State the preparation type.
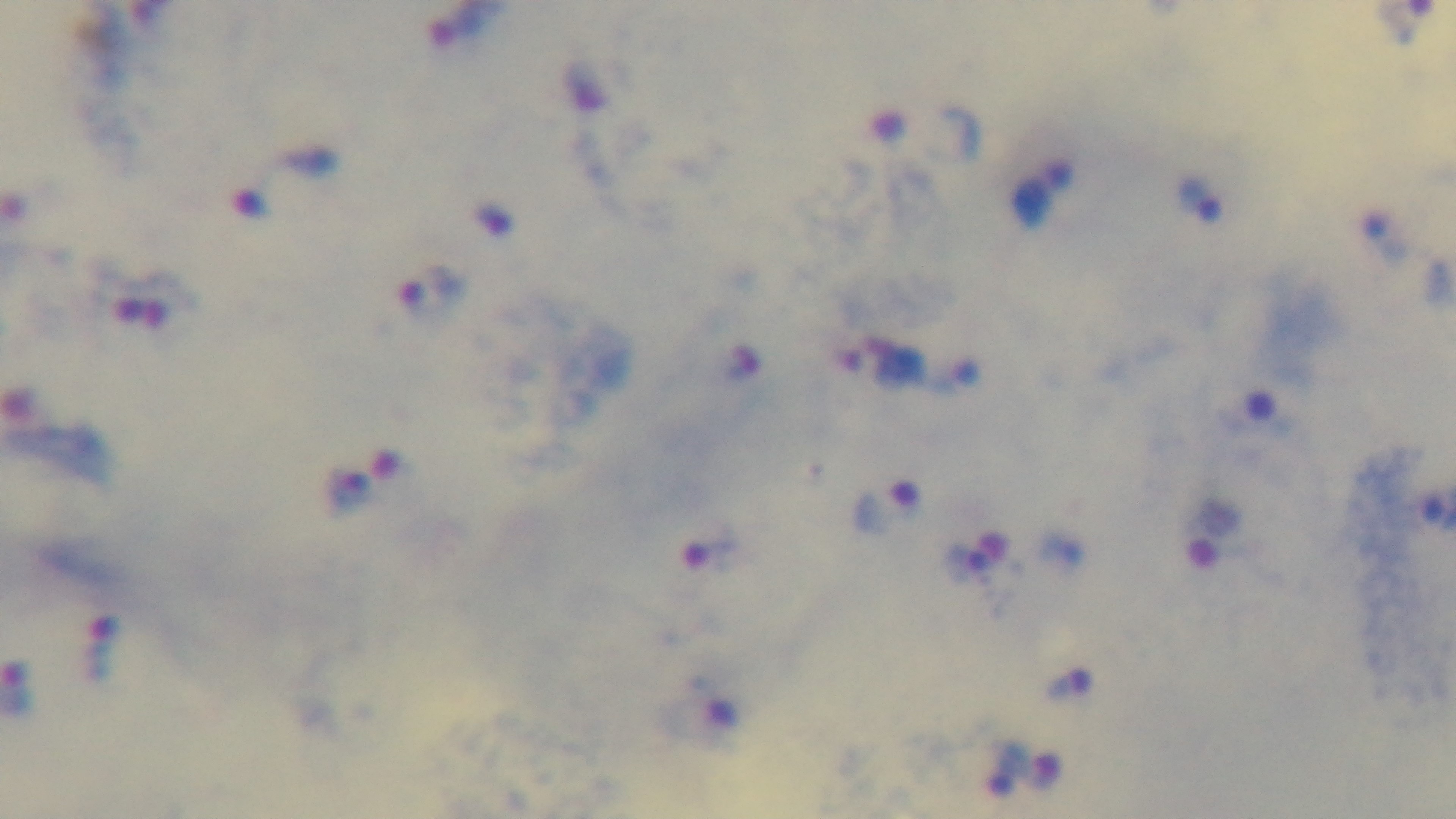

It is a thick blood film.

stain = Giemsa
objective = 100x oil immersion
malaria status = positive
modality = light microscopy
field of view = single
capture = mounted 4K digital camera